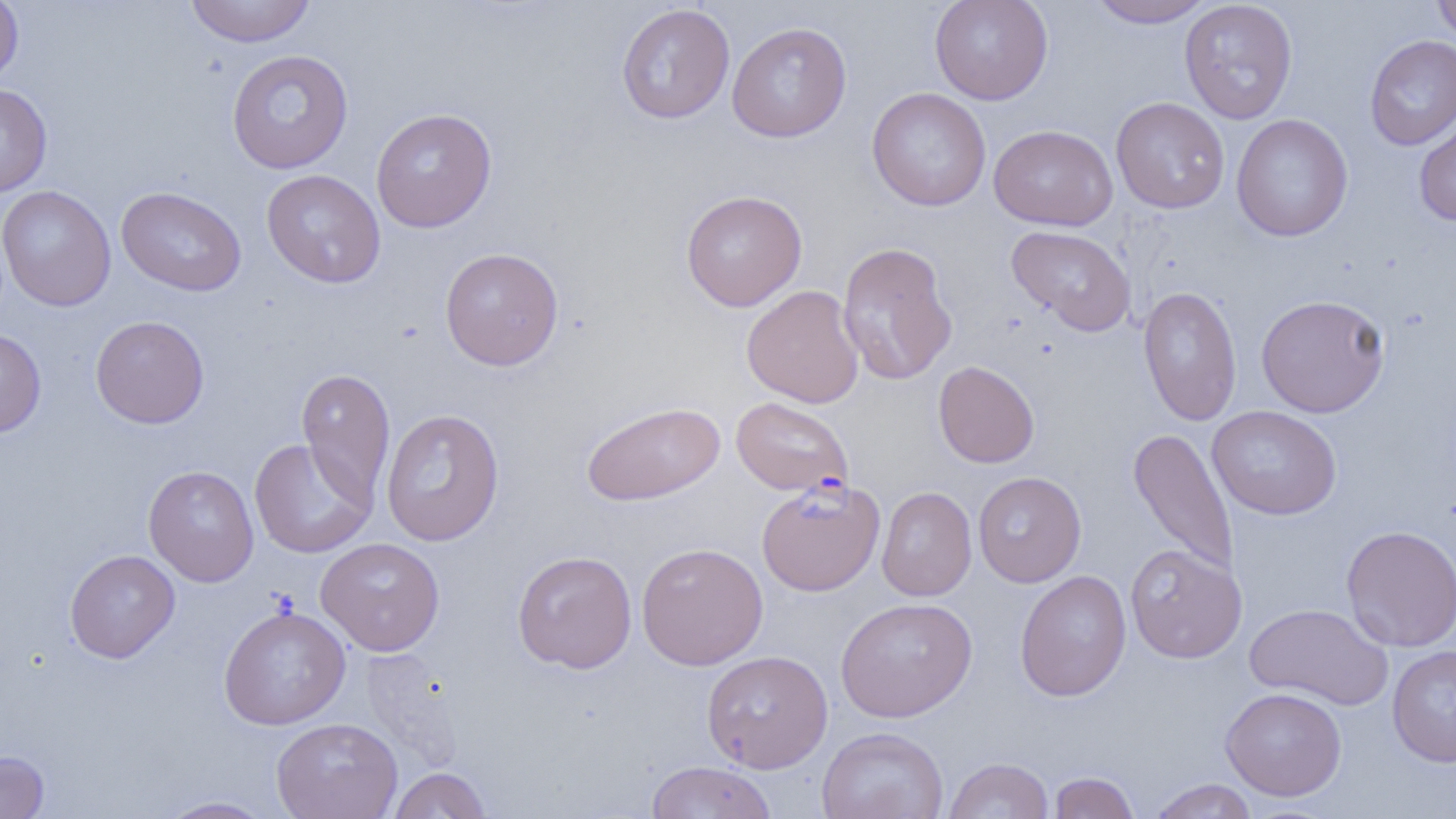

Approximate bounding boxes as named x1/y1/x2/y2 corners in pixels. Uninfected red blood cell locations: (x1=0, y1=0, x2=23, y2=87), (x1=183, y1=0, x2=318, y2=47), (x1=929, y1=0, x2=1054, y2=105), (x1=1085, y1=0, x2=1216, y2=28), (x1=1179, y1=0, x2=1298, y2=124), (x1=1431, y1=0, x2=1456, y2=45), (x1=616, y1=3, x2=735, y2=124), (x1=726, y1=22, x2=852, y2=143), (x1=1364, y1=34, x2=1456, y2=151), (x1=226, y1=49, x2=354, y2=174), (x1=0, y1=84, x2=53, y2=198), (x1=867, y1=87, x2=991, y2=212), (x1=1110, y1=97, x2=1230, y2=214), (x1=370, y1=107, x2=497, y2=233), (x1=1413, y1=107, x2=1456, y2=226), (x1=1231, y1=113, x2=1353, y2=241), (x1=989, y1=124, x2=1118, y2=231), (x1=261, y1=169, x2=386, y2=288), (x1=0, y1=185, x2=116, y2=311), (x1=116, y1=186, x2=247, y2=296), (x1=680, y1=189, x2=808, y2=312), (x1=1006, y1=225, x2=1137, y2=337), (x1=836, y1=241, x2=958, y2=386), (x1=439, y1=247, x2=564, y2=371), (x1=741, y1=285, x2=864, y2=408), (x1=1138, y1=286, x2=1242, y2=425), (x1=1256, y1=294, x2=1390, y2=417), (x1=90, y1=315, x2=209, y2=429), (x1=0, y1=328, x2=46, y2=438), (x1=933, y1=360, x2=1040, y2=468), (x1=296, y1=368, x2=396, y2=506), (x1=731, y1=396, x2=854, y2=497), (x1=581, y1=400, x2=726, y2=506), (x1=1207, y1=405, x2=1342, y2=520), (x1=380, y1=408, x2=505, y2=546), (x1=1127, y1=427, x2=1239, y2=578), (x1=249, y1=438, x2=376, y2=559), (x1=143, y1=465, x2=259, y2=587), (x1=973, y1=471, x2=1086, y2=587), (x1=876, y1=486, x2=977, y2=601), (x1=1341, y1=524, x2=1456, y2=652), (x1=315, y1=537, x2=445, y2=655), (x1=636, y1=542, x2=768, y2=670), (x1=1124, y1=544, x2=1247, y2=663), (x1=64, y1=549, x2=180, y2=663), (x1=512, y1=550, x2=637, y2=673), (x1=1014, y1=570, x2=1132, y2=701), (x1=835, y1=597, x2=978, y2=722), (x1=218, y1=604, x2=351, y2=729), (x1=1244, y1=604, x2=1394, y2=710), (x1=1387, y1=644, x2=1456, y2=767), (x1=359, y1=649, x2=466, y2=771), (x1=702, y1=649, x2=833, y2=773), (x1=1220, y1=687, x2=1347, y2=801), (x1=271, y1=717, x2=403, y2=819), (x1=817, y1=727, x2=949, y2=819), (x1=0, y1=750, x2=49, y2=819), (x1=944, y1=757, x2=1054, y2=819), (x1=645, y1=761, x2=777, y2=818), (x1=388, y1=767, x2=491, y2=818), (x1=1049, y1=771, x2=1139, y2=818), (x1=1147, y1=778, x2=1258, y2=819), (x1=157, y1=795, x2=277, y2=818). Plasmodium falciparum-infected red blood cell locations: (x1=756, y1=478, x2=885, y2=596). Slide-level diagnosis: Plasmodium falciparum. One field of a larger specimen. Captured at 1000x magnification. Thin blood smear. Image is 1456×819 pixels. Light microscopy.